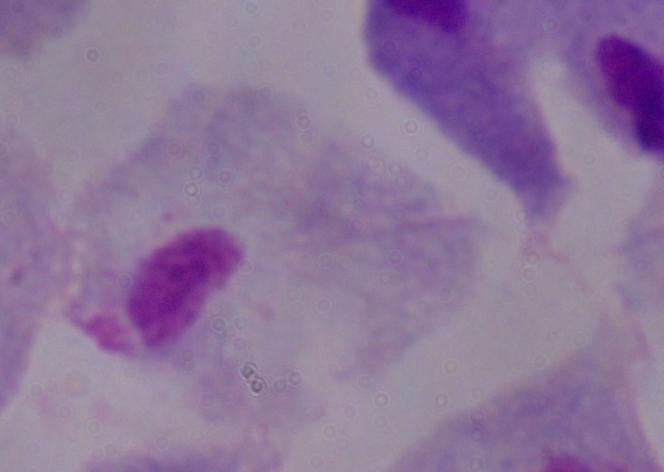

Captured at 1000x magnification. Photomicrograph. A trichomonad is seen.